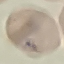

Summary:
  - Malaria status: uninfected
  - Stain: Giemsa
  - Capture: smartphone through the microscope eyepiece
  - Image type: cell patch, automatically extracted from a larger field of view and resized to 64 × 64 pixels
  - Preparation: thin blood smear